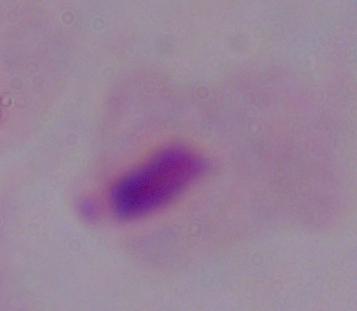
Photomicrograph. A trichomonad is shown. Captured at 1000x magnification.